Comment on the morphology of the red blood cells.
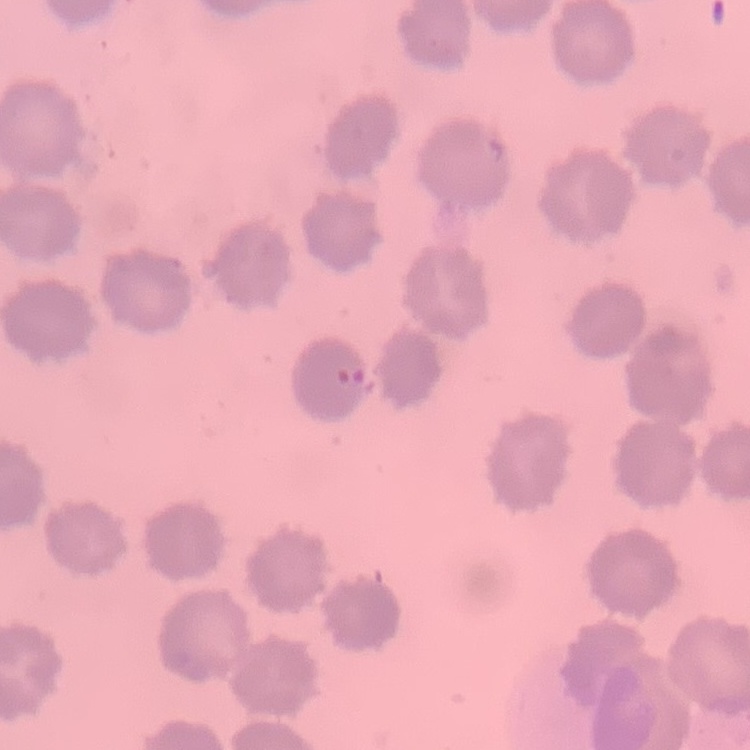

No rouleaux formation.

Square crop of a larger photomicrograph. Field's or Giemsa stain. Thin peripheral smear.